Report the malaria status of this cell.
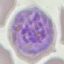
It is parasitized.

Summary:
  - Image type: automatically extracted cell patch, resized to 64 × 64 pixels
  - Capture: smartphone camera at the microscope eyepiece
  - Preparation: thin blood smear
  - Stain: Giemsa